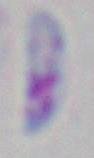

Summary:
  - Modality: photomicrograph
  - Magnification: 1000x
  - Identification: Toxoplasma gondii